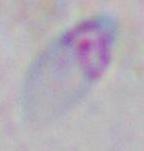

Summary:
  - Modality: micrograph
  - Magnification: 1000x
  - Identification: Toxoplasma gondii